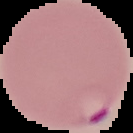
Summary:
  - Image size: 133×133 pixels
  - Image type: segmented cell region with the area outside set to black
  - Preparation: thin blood film
  - Result: malaria parasites identified